Assess the morphology of the erythrocytes.
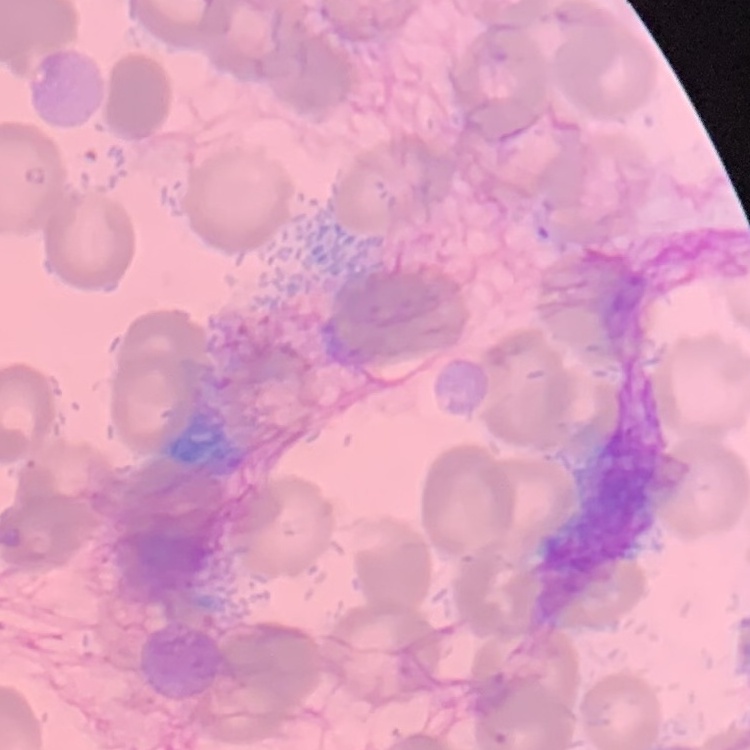
No rouleaux formation.

{
  "preparation": "thin blood film",
  "stain": "Field's or Giemsa",
  "image_type": "one tile cut from a larger photomicrograph"
}